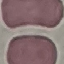

Summary:
  - Result: negative for malaria parasites
  - Image type: cell patch, automatically extracted from a larger field of view and resized to 64 × 64 pixels
  - Capture: smartphone through the microscope eyepiece
  - Stain: Giemsa
  - Preparation: thin smear